Locate every leukocyte (white blood cell).
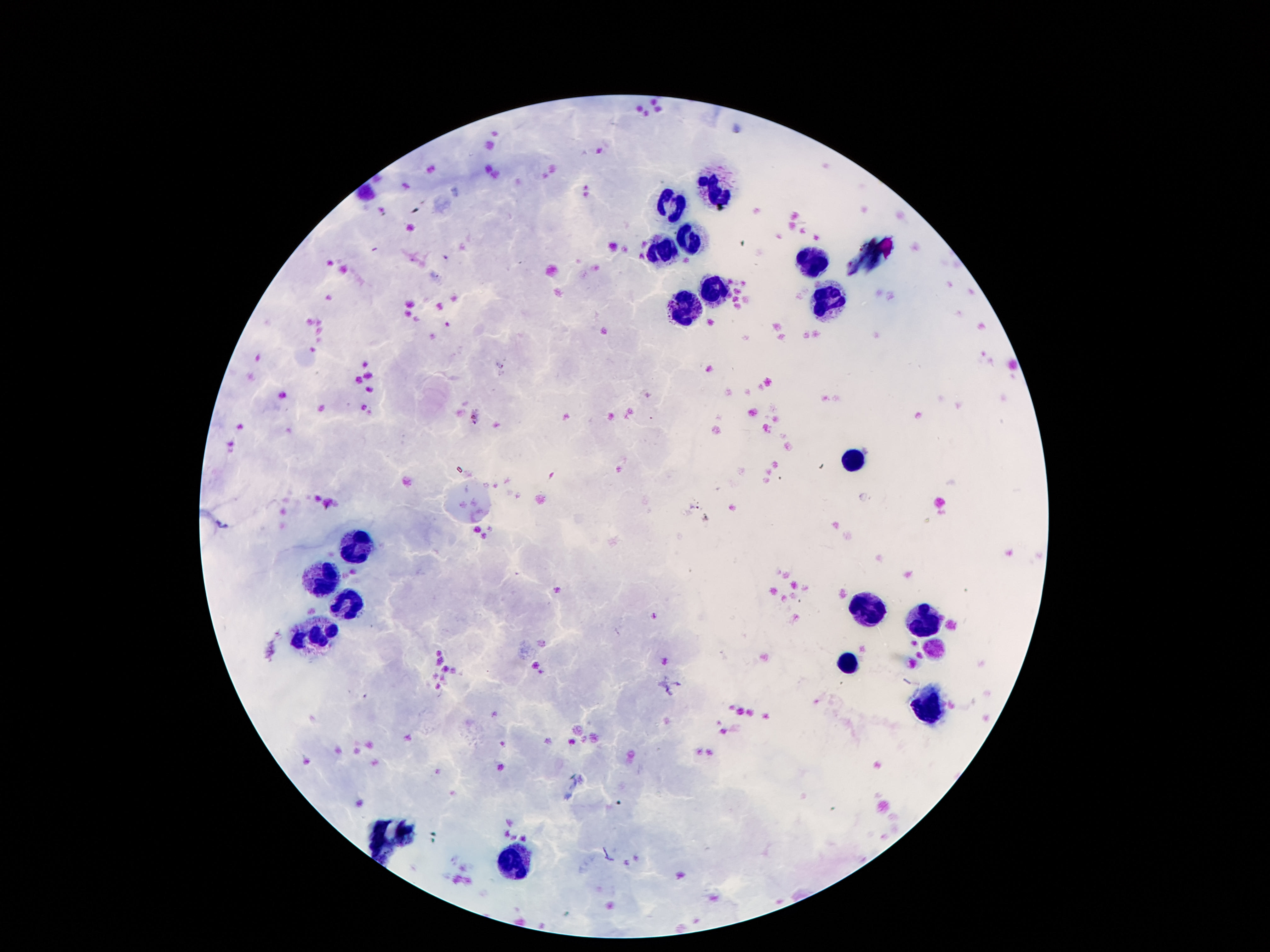
Approximate centers as [x, y] in pixels.
Leukocytes: [717, 190], [672, 199], [688, 239], [663, 251], [809, 261], [713, 288], [682, 306], [829, 307], [848, 458], [360, 550], [326, 581], [348, 603], [862, 607], [925, 628], [319, 634], [848, 666], [926, 708], [516, 861].

Summary:
  - Magnification: 100x
  - Capture: smartphone camera through the microscope eyepiece
  - Stain: Giemsa
  - Image size: 1270×952 pixels
  - Preparation: thick blood smear
  - Patient malaria status: negative
  - Field of view: single